Report the malaria status of this cell.
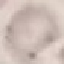
It is uninfected.

Acquired by smartphone through the microscope eyepiece. Automatically extracted cell patch, resized to 64 × 64 pixels. Thin smear of blood. Giemsa stain.